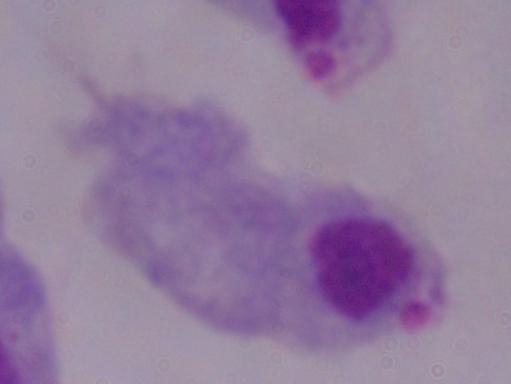
Summary:
  - Magnification: 1000x
  - Identification: trichomonad
  - Modality: photomicrograph